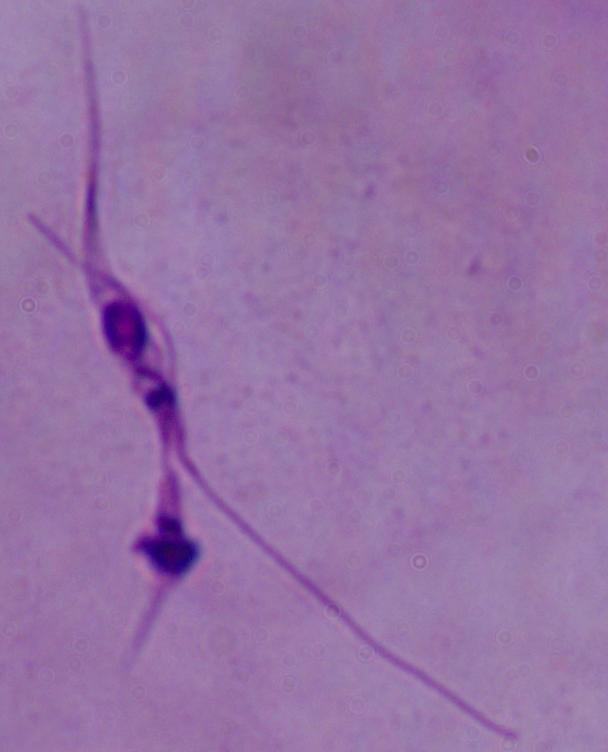

Summary:
  - Identification: Leishmania
  - Magnification: 1000x
  - Modality: micrograph